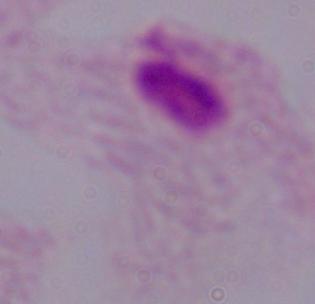 Micrograph. A trichomonad is seen. Captured at 1000x magnification.